Identify the parasite.
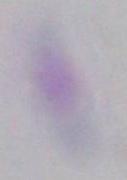

Toxoplasma gondii.

Captured at 1000x magnification. Photomicrograph.